Name the blood parasite species.
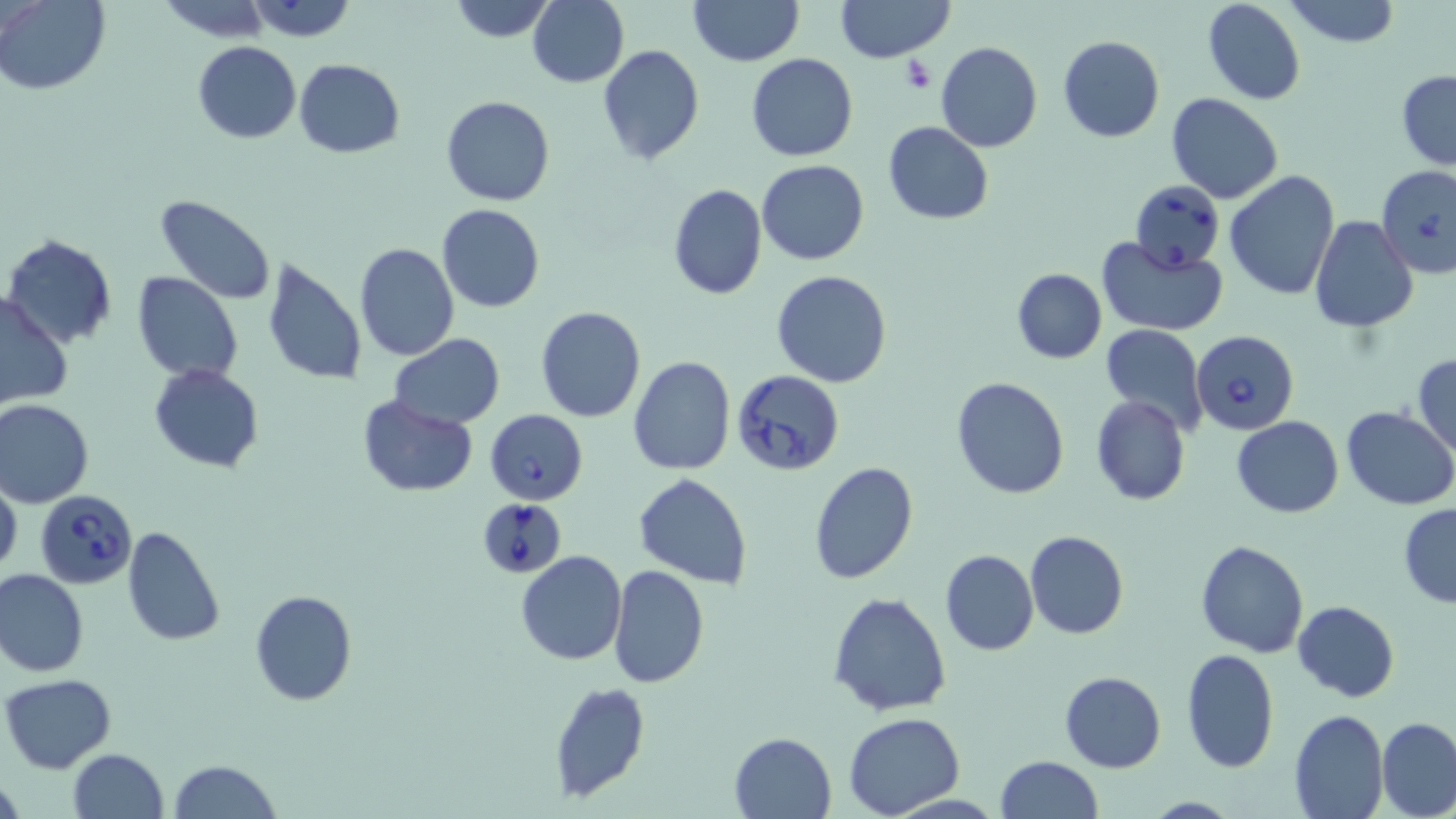

Babesia divergens.

magnification = 1000x
Babesia divergens-infected red blood cell locations = approximate bounding boxes as named x1/y1/x2/y2 corners in pixels: (x1=1376, y1=162, x2=1455, y2=277), (x1=1130, y1=179, x2=1225, y2=273), (x1=1191, y1=329, x2=1300, y2=436), (x1=731, y1=369, x2=844, y2=478), (x1=484, y1=409, x2=589, y2=506), (x1=36, y1=490, x2=137, y2=588), (x1=475, y1=494, x2=568, y2=579)
stain = May-Grünwald-Giemsa
platelet locations = approximate bounding boxes as named x1/y1/x2/y2 corners in pixels: (x1=900, y1=58, x2=937, y2=94)
uninfected red blood cell locations = approximate bounding boxes as named x1/y1/x2/y2 corners in pixels: (x1=0, y1=0, x2=110, y2=94), (x1=156, y1=0, x2=274, y2=41), (x1=447, y1=0, x2=554, y2=42), (x1=528, y1=0, x2=628, y2=88), (x1=687, y1=0, x2=801, y2=66), (x1=835, y1=0, x2=954, y2=63), (x1=1202, y1=0, x2=1305, y2=105), (x1=1285, y1=0, x2=1401, y2=48), (x1=245, y1=1, x2=360, y2=44), (x1=1057, y1=35, x2=1165, y2=143), (x1=191, y1=41, x2=301, y2=143), (x1=936, y1=42, x2=1042, y2=152), (x1=598, y1=45, x2=705, y2=165), (x1=745, y1=53, x2=859, y2=162), (x1=293, y1=58, x2=405, y2=158), (x1=1396, y1=69, x2=1456, y2=171), (x1=1165, y1=92, x2=1285, y2=204), (x1=441, y1=95, x2=554, y2=206), (x1=884, y1=121, x2=994, y2=224), (x1=757, y1=160, x2=869, y2=265), (x1=1224, y1=170, x2=1340, y2=300), (x1=666, y1=184, x2=767, y2=300), (x1=153, y1=196, x2=276, y2=306), (x1=435, y1=203, x2=545, y2=313), (x1=1309, y1=216, x2=1418, y2=333), (x1=1, y1=235, x2=118, y2=350), (x1=1096, y1=235, x2=1227, y2=335), (x1=354, y1=244, x2=459, y2=362), (x1=260, y1=256, x2=369, y2=386), (x1=1012, y1=267, x2=1106, y2=362), (x1=772, y1=269, x2=891, y2=389), (x1=132, y1=271, x2=244, y2=384), (x1=0, y1=292, x2=73, y2=412), (x1=536, y1=306, x2=646, y2=422), (x1=1099, y1=324, x2=1209, y2=433), (x1=389, y1=333, x2=506, y2=429), (x1=1413, y1=353, x2=1456, y2=456), (x1=628, y1=357, x2=736, y2=476), (x1=149, y1=363, x2=264, y2=473), (x1=950, y1=375, x2=1070, y2=500), (x1=356, y1=394, x2=478, y2=497), (x1=1090, y1=395, x2=1190, y2=507), (x1=0, y1=398, x2=95, y2=507), (x1=1340, y1=406, x2=1456, y2=511), (x1=1231, y1=416, x2=1344, y2=517), (x1=809, y1=462, x2=918, y2=585), (x1=634, y1=474, x2=752, y2=589), (x1=0, y1=475, x2=22, y2=582), (x1=1398, y1=504, x2=1456, y2=607), (x1=119, y1=526, x2=226, y2=646), (x1=1025, y1=530, x2=1130, y2=640), (x1=1193, y1=539, x2=1309, y2=658), (x1=940, y1=549, x2=1038, y2=656), (x1=516, y1=550, x2=627, y2=665), (x1=610, y1=564, x2=709, y2=687), (x1=0, y1=568, x2=88, y2=678), (x1=249, y1=589, x2=358, y2=706), (x1=828, y1=592, x2=953, y2=717), (x1=1293, y1=599, x2=1399, y2=703), (x1=1179, y1=648, x2=1280, y2=772), (x1=1059, y1=671, x2=1166, y2=774), (x1=1, y1=674, x2=118, y2=775), (x1=548, y1=682, x2=651, y2=803), (x1=1287, y1=708, x2=1389, y2=819), (x1=842, y1=712, x2=965, y2=819), (x1=1376, y1=717, x2=1456, y2=819), (x1=729, y1=730, x2=836, y2=817), (x1=67, y1=749, x2=169, y2=819), (x1=997, y1=756, x2=1103, y2=818), (x1=170, y1=759, x2=280, y2=818), (x1=0, y1=772, x2=24, y2=819), (x1=1141, y1=796, x2=1245, y2=818)
image size = 1456×819 pixels
modality = light microscopy
preparation = thin blood film
field of view = single